State the blood parasite species.
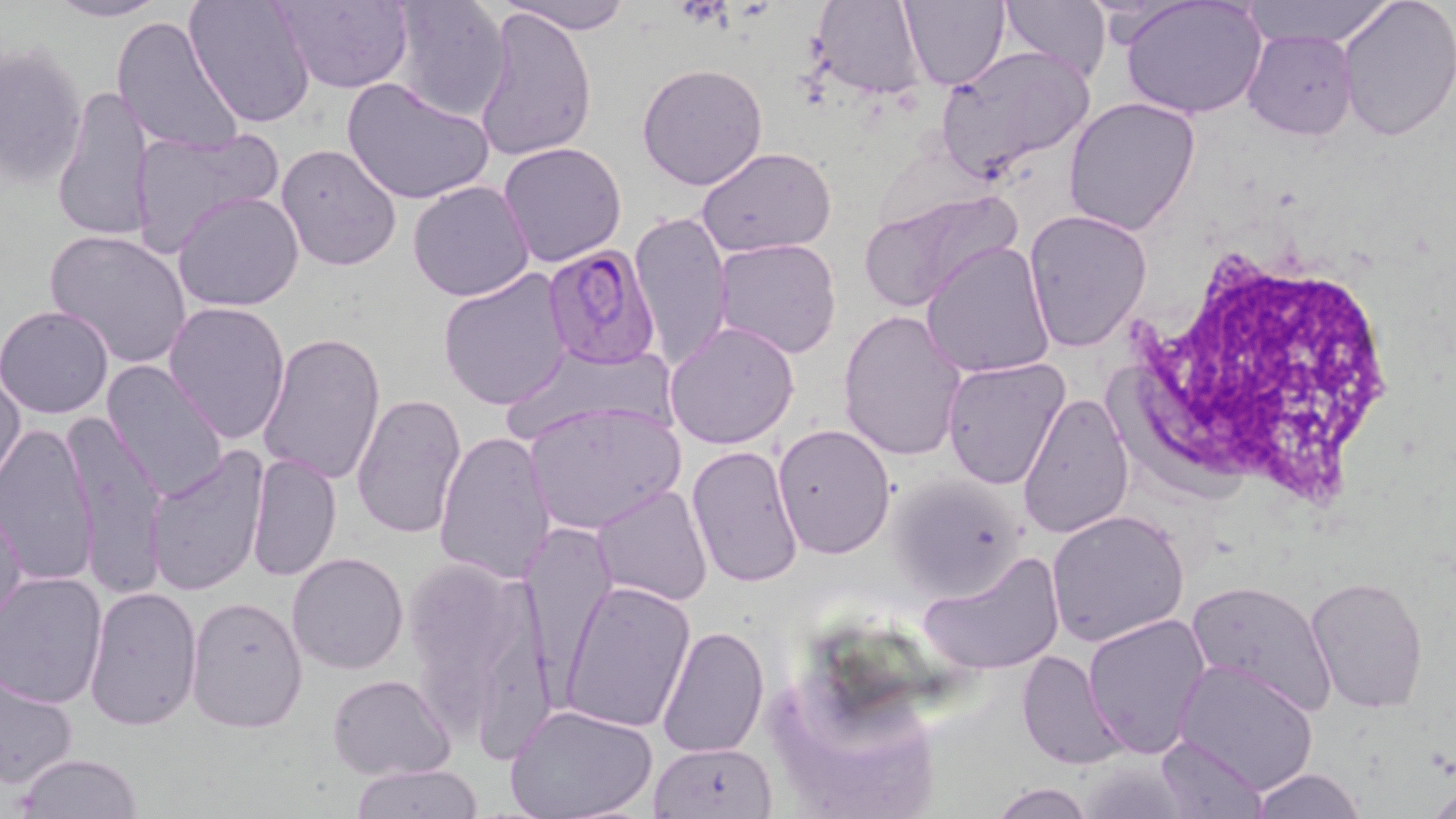
Plasmodium falciparum.

Summary:
  - Coordinate format: approximate bounding boxes as [x1, y1, x2, y2] in pixels
  - Plasmodium falciparum-infected red blood cell locations: [540, 243, 661, 368]
  - White blood cell locations: [1117, 236, 1401, 503]
  - Uninfected red blood cell locations: [44, 0, 169, 23], [183, 0, 316, 127], [272, 0, 414, 91], [385, 0, 510, 123], [500, 0, 631, 35], [810, 0, 928, 99], [900, 0, 1011, 92], [999, 0, 1112, 84], [1121, 0, 1267, 120], [1240, 0, 1396, 49], [1336, 0, 1456, 143], [474, 8, 597, 161], [111, 16, 245, 156], [1243, 30, 1357, 141], [0, 39, 88, 192], [933, 44, 1096, 184], [637, 63, 769, 191], [343, 76, 496, 208], [51, 85, 157, 243], [1064, 96, 1201, 236], [127, 124, 282, 257], [498, 141, 627, 267], [276, 143, 402, 271], [697, 146, 838, 258], [406, 180, 535, 302], [859, 188, 1019, 316], [173, 190, 305, 312], [1023, 208, 1152, 353], [629, 211, 735, 371], [44, 229, 193, 371], [712, 237, 842, 359], [922, 240, 1057, 377], [437, 269, 575, 411], [162, 298, 292, 443], [0, 305, 117, 418], [837, 310, 967, 462], [664, 320, 802, 449], [257, 332, 386, 486], [504, 339, 679, 441], [941, 357, 1071, 489], [102, 359, 232, 501], [0, 366, 25, 487], [351, 393, 468, 541], [1018, 394, 1133, 538], [522, 400, 685, 535], [62, 412, 168, 595], [0, 422, 101, 592], [771, 423, 894, 560], [435, 430, 559, 586], [686, 445, 804, 590], [145, 448, 270, 600], [247, 452, 341, 583], [887, 474, 1027, 599], [591, 483, 712, 608], [1, 503, 27, 632], [1046, 510, 1189, 647], [518, 526, 617, 674], [400, 551, 557, 753], [918, 551, 1065, 676], [287, 553, 411, 675], [0, 570, 108, 709], [1304, 575, 1430, 714], [1187, 580, 1336, 717], [560, 581, 696, 733], [82, 584, 202, 731], [186, 594, 308, 733], [1083, 613, 1211, 758], [657, 623, 770, 758], [1016, 649, 1128, 769], [1173, 659, 1320, 794], [0, 673, 80, 790], [328, 673, 455, 781], [506, 703, 659, 819], [1155, 734, 1269, 819], [648, 742, 779, 819], [12, 752, 144, 818], [350, 763, 484, 819], [1249, 767, 1366, 819], [986, 780, 1097, 818]
  - Preparation: thin blood film
  - Modality: optical microscopy
  - Field of view: one of a larger specimen
  - Stain: May-Grünwald-Giemsa
  - Magnification: 1000x
  - Image size: 1456×819 pixels